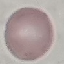 Malaria status: uninfected. Automatically extracted cell patch, resized to 64 × 64 pixels. Thin smear of blood. Giemsa stain. Photographed with a smartphone camera at the microscope eyepiece.